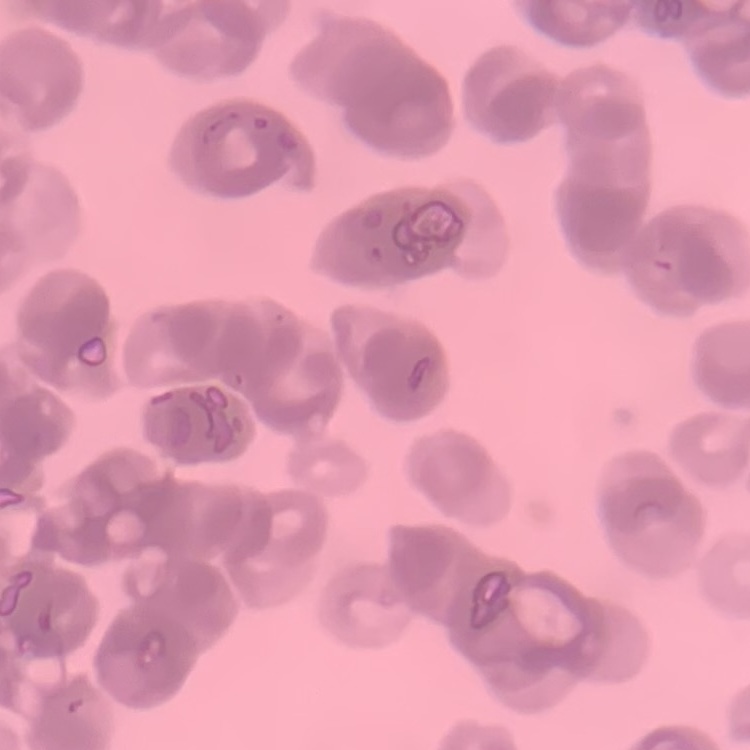

Summary:
  - Red blood cell morphology: rouleaux formation
  - Image type: square crop of a larger photomicrograph
  - Stain: Field's or Giemsa
  - Preparation: thin blood film